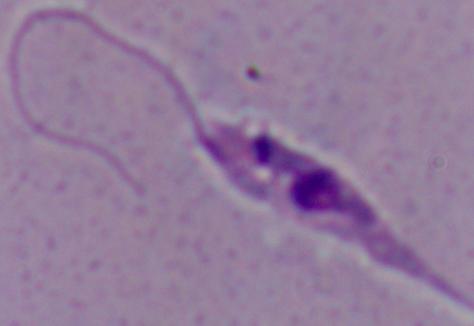

magnification = 1000x
modality = micrograph
identification = Leishmania